State which cell type is depicted.
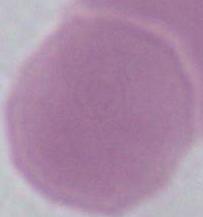

An erythrocyte.

1000x magnification. Micrograph.